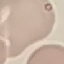
Summary:
  - Malaria status: uninfected
  - Stain: Giemsa
  - Image type: cell patch, automatically extracted from a larger field of view and resized to 64 × 64 pixels
  - Capture: smartphone camera at the microscope eyepiece
  - Preparation: thin blood smear